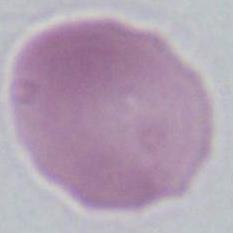
Summary:
  - Identification: red blood cell
  - Magnification: 1000x
  - Modality: micrograph